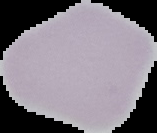
Segmented cell region on a black background. Malaria status: uninfected. Image is 157×133 pixels. From a thin blood film.